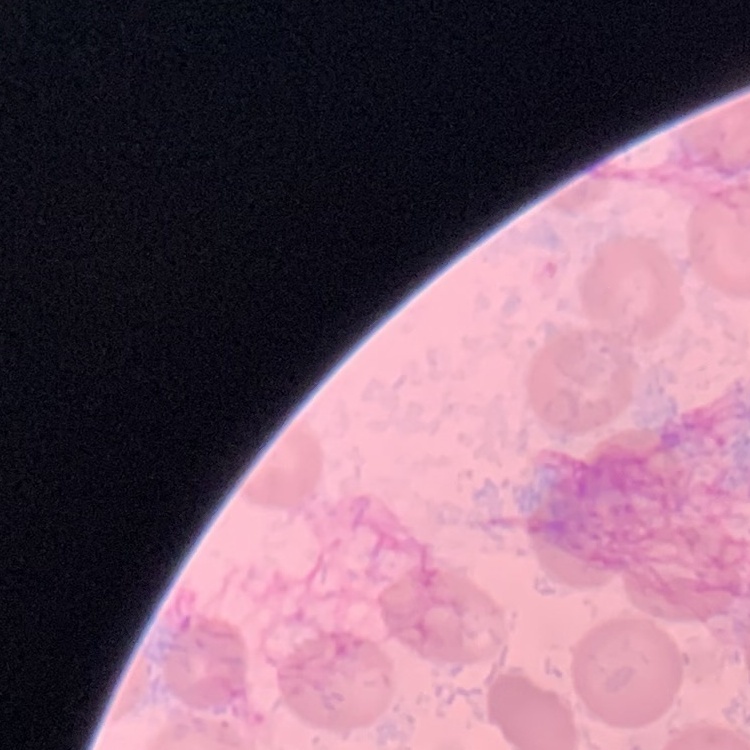 The red blood cells exhibit no rouleaux formation. Thin peripheral smear. Square crop of a larger photomicrograph. Stained with either Field's or Giemsa.